Classify this cell by malaria status.
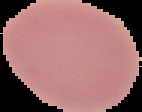
It is uninfected.

Summary:
  - Image size: 142×112 pixels
  - Image type: segmented cell region with the area outside set to black
  - Preparation: thin blood smear